State which cell type is depicted.
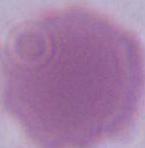

This is an erythrocyte.

Summary:
  - Magnification: 1000x
  - Modality: photomicrograph